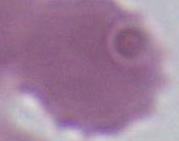
Summary:
  - Modality: photomicrograph
  - Magnification: 1000x
  - Identification: erythrocyte